State the preparation type.
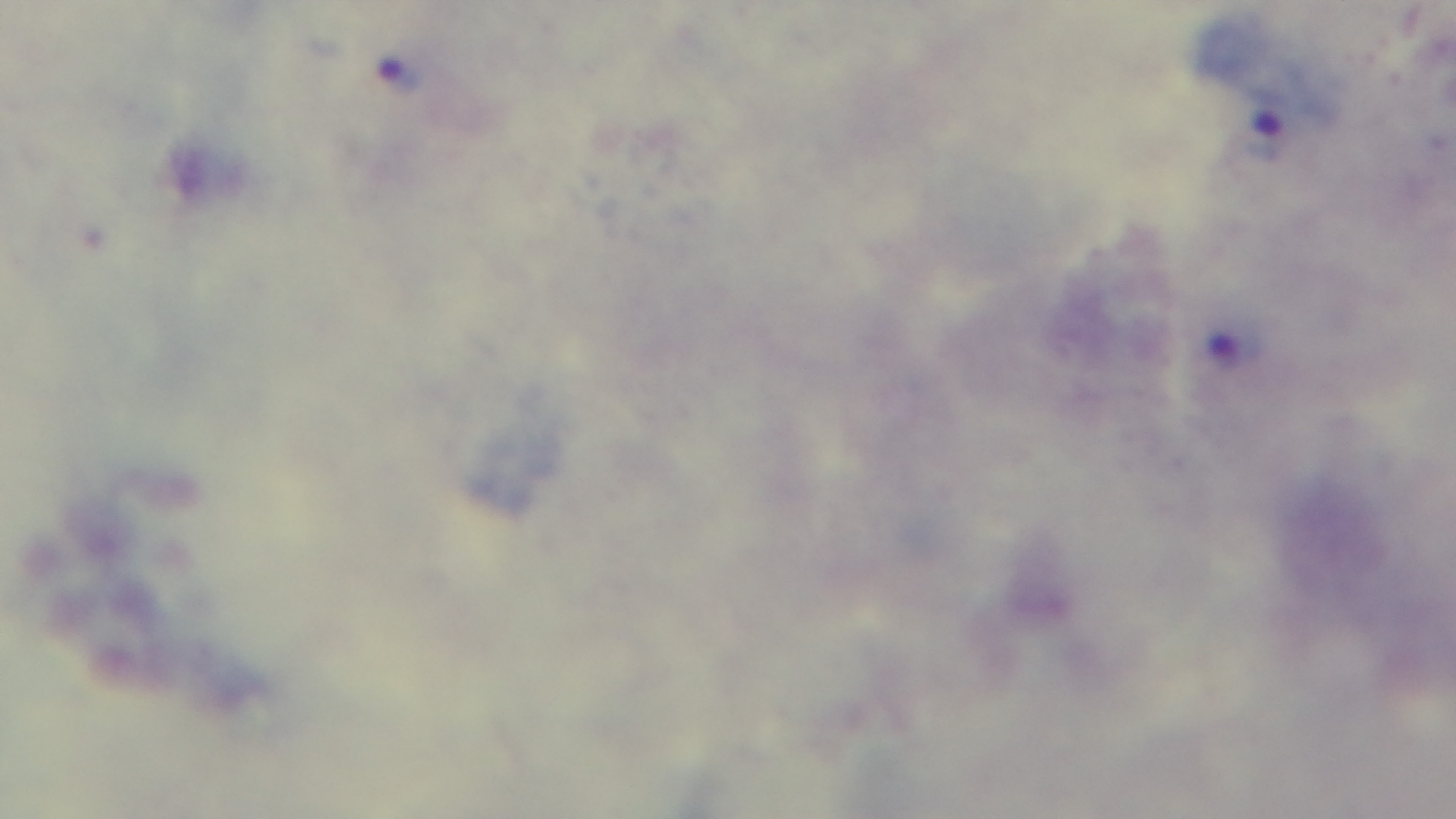

It is a thick blood film.

stain = Giemsa
objective = 100x oil immersion
malaria status = infected
field of view = single
capture = mounted 4K digital camera
modality = light microscopy